Name the parasite shown.
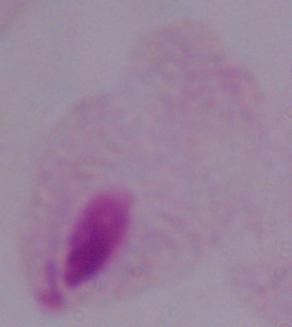

This is a trichomonad.

Micrograph. Captured at 1000x magnification.